Give the position of every Plasmodium parasite visible.
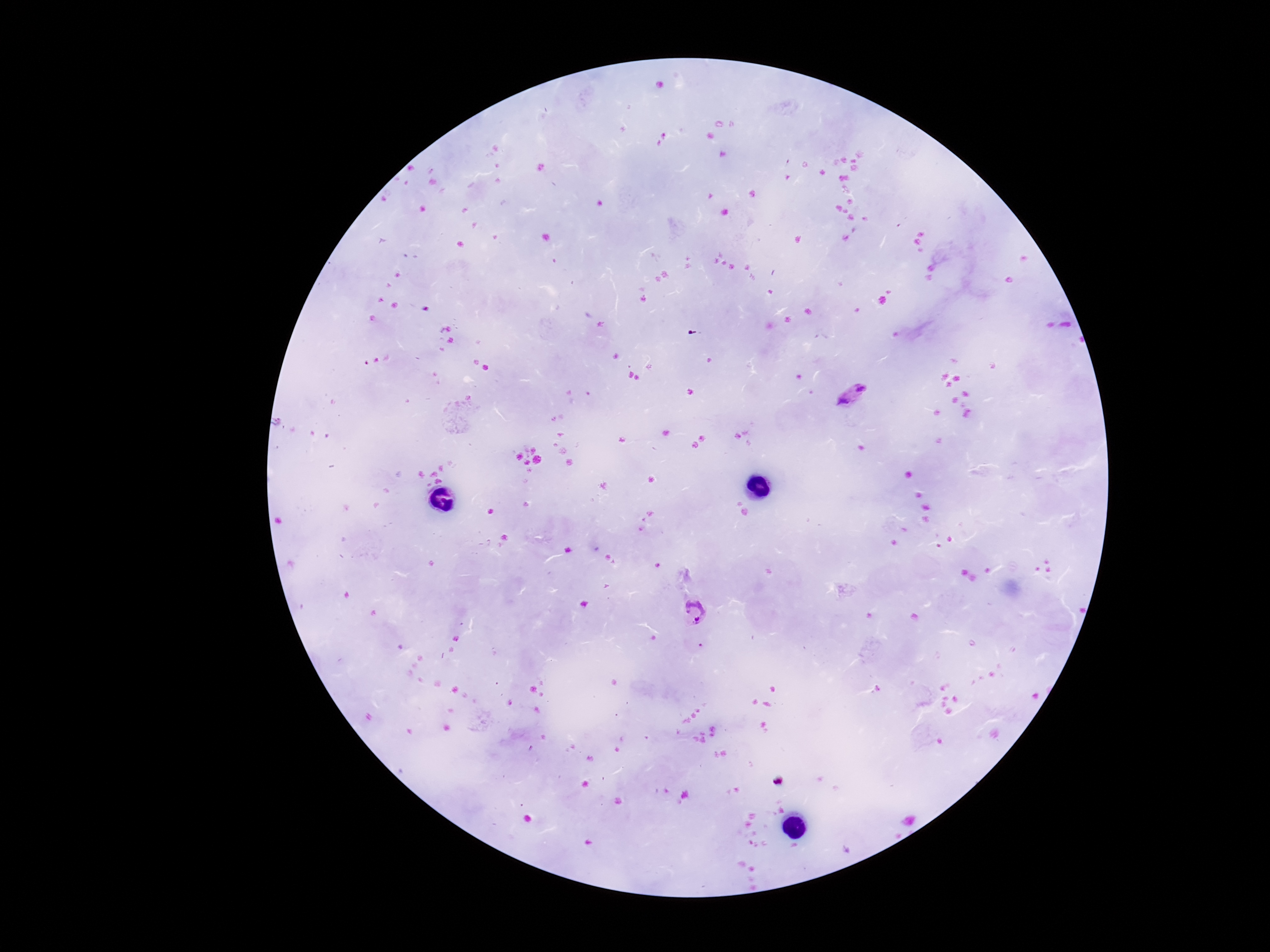
Approximate centers as {x, y} in pixels.
Plasmodium parasites: {861, 388}, {844, 401}, {695, 610}.

Summary:
  - Patient malaria status: positive
  - Capture: smartphone camera through the microscope eyepiece
  - Field of view: single
  - Stain: Giemsa
  - Image size: 1270×952 pixels
  - Preparation: thick peripheral-blood smear
  - Magnification: 100x